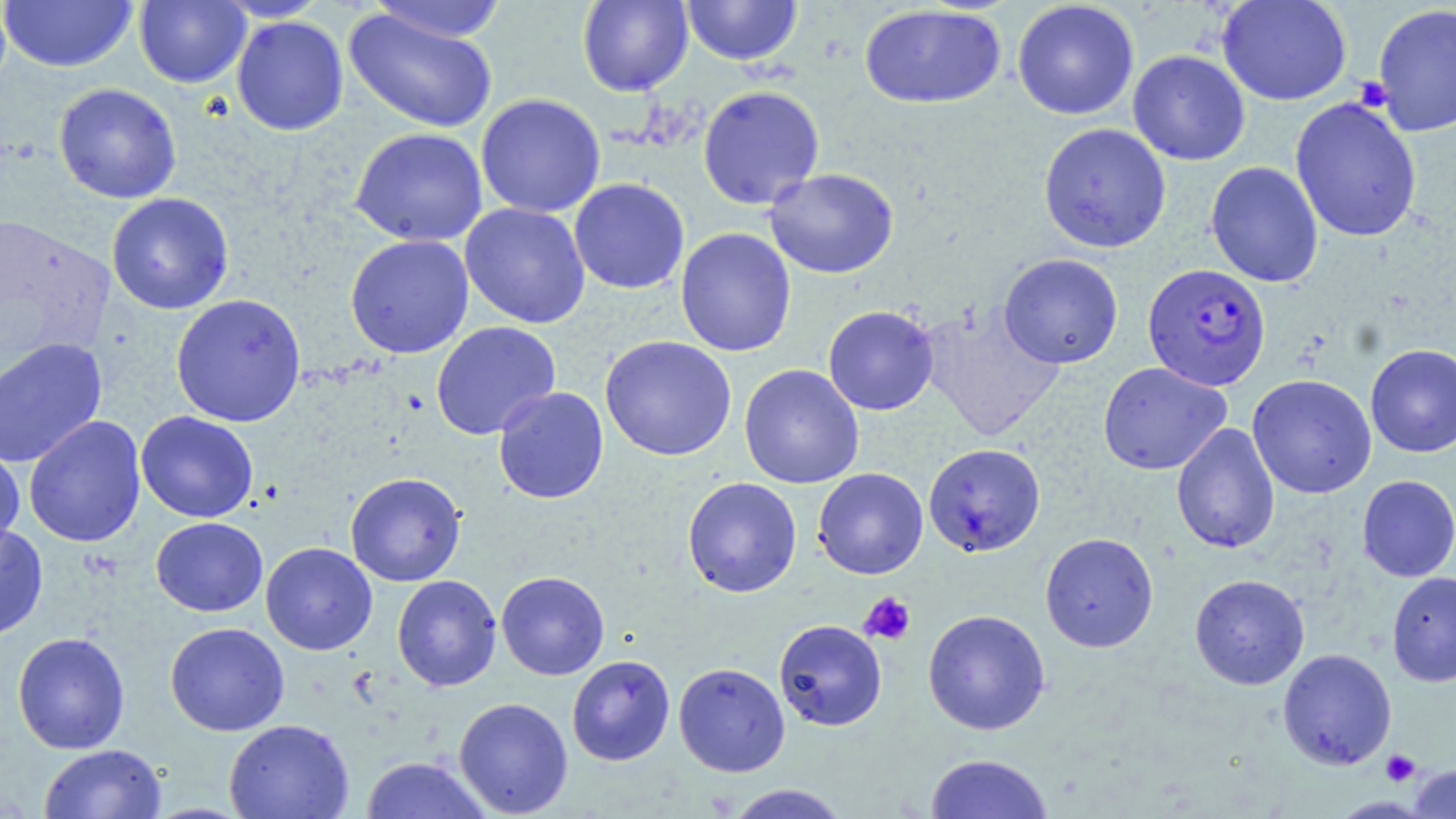
Summary:
  - Coordinate format: approximate bounding boxes as [x1, y1, x2, y2] in pixels
  - Plasmodium falciparum-infected red blood cell locations: [1142, 263, 1271, 390]
  - Uninfected red blood cell locations: [0, 0, 138, 73], [364, 0, 510, 43], [577, 0, 693, 96], [681, 0, 803, 66], [1216, 0, 1352, 106], [134, 1, 251, 88], [1011, 1, 1140, 120], [1372, 3, 1456, 137], [858, 4, 1006, 109], [342, 8, 499, 134], [231, 16, 349, 136], [1127, 50, 1250, 166], [53, 83, 181, 204], [697, 85, 825, 210], [475, 93, 606, 218], [1290, 96, 1422, 243], [1038, 123, 1171, 253], [350, 127, 488, 247], [1205, 161, 1323, 287], [764, 168, 899, 278], [569, 178, 690, 295], [106, 193, 234, 315], [460, 203, 591, 329], [675, 228, 797, 357], [345, 234, 474, 358], [998, 253, 1123, 369], [170, 294, 306, 427], [920, 303, 1065, 443], [823, 305, 940, 415], [431, 321, 561, 440], [599, 336, 737, 461], [0, 338, 108, 468], [1365, 344, 1456, 457], [1098, 362, 1231, 475], [738, 364, 864, 489], [1247, 373, 1376, 498], [493, 386, 608, 504], [135, 411, 259, 523], [24, 415, 146, 548], [1171, 422, 1280, 554], [924, 443, 1046, 556], [0, 444, 25, 554], [813, 467, 928, 579], [345, 472, 466, 587], [1357, 475, 1456, 581], [682, 477, 802, 598], [151, 517, 268, 617], [0, 523, 49, 641], [1039, 532, 1159, 652], [261, 542, 377, 655], [1387, 570, 1456, 687], [496, 571, 609, 680], [1190, 574, 1309, 689], [392, 575, 502, 691], [923, 609, 1050, 735], [774, 619, 887, 731], [165, 622, 289, 736], [12, 631, 130, 754], [1278, 648, 1397, 769], [567, 655, 675, 765], [673, 662, 790, 776], [453, 697, 573, 817], [224, 719, 353, 819], [38, 743, 166, 819], [925, 752, 1053, 819], [361, 756, 492, 818], [1408, 764, 1456, 818], [723, 784, 850, 818]
  - Platelet locations: [1354, 75, 1394, 111], [859, 591, 916, 645], [1381, 749, 1420, 787]
  - Slide-level diagnosis: Plasmodium falciparum
  - Magnification: 1000x
  - Image size: 1456×819 pixels
  - Preparation: thin blood film
  - Stain: May-Grünwald-Giemsa
  - Field of view: single
  - Modality: light microscopy